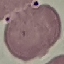
{
  "result": "negative for malaria parasites",
  "preparation": "thin blood smear",
  "stain": "Giemsa",
  "capture": "smartphone through the microscope eyepiece",
  "image_type": "automatically extracted cell patch, resized to 64 × 64 pixels"
}